Assess this cell for malaria.
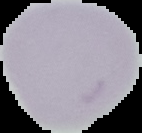
It is uninfected.

preparation: thin blood film
image_size: 142×133 pixels
image_type: segmented cell region on a black background